Locate every blood parasite and identify its species.
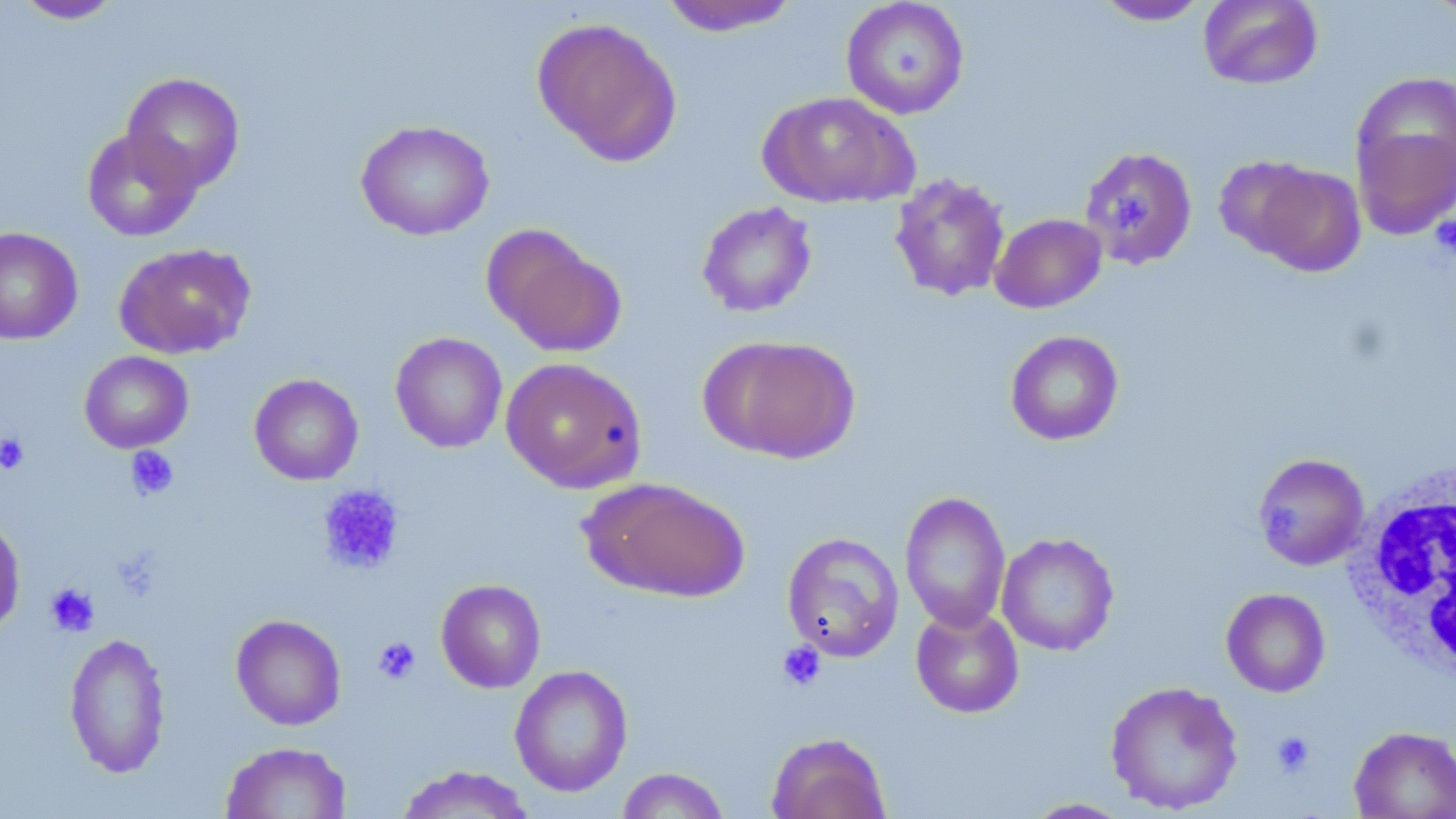
No blood parasites observed.

Approximate bounding boxes as [x1, y1, x2, y2] in pixels. Platelet locations: [1118, 192, 1161, 242], [1431, 214, 1456, 258], [0, 431, 30, 475], [126, 446, 178, 500], [317, 484, 405, 576], [44, 583, 99, 636], [373, 637, 420, 685], [777, 641, 826, 691], [1270, 730, 1316, 778]. Uninfected red blood cell locations: [12, 0, 125, 24], [1198, 0, 1324, 90], [657, 1, 804, 36], [841, 1, 970, 120], [1092, 1, 1211, 26], [532, 17, 682, 166], [122, 72, 244, 193], [1351, 89, 1456, 238], [758, 91, 916, 209], [355, 119, 494, 241], [82, 127, 202, 241], [1079, 146, 1198, 271], [1234, 159, 1366, 277], [889, 173, 1011, 302], [697, 202, 817, 317], [990, 213, 1107, 313], [481, 224, 625, 357], [0, 227, 83, 345], [113, 242, 256, 360], [1005, 330, 1124, 446], [390, 332, 508, 453], [700, 334, 860, 463], [79, 351, 193, 453], [500, 357, 647, 493], [249, 374, 363, 486], [1252, 453, 1370, 571], [582, 476, 750, 603], [899, 490, 1011, 633], [0, 515, 25, 638], [782, 532, 904, 662], [997, 532, 1119, 656], [436, 579, 546, 693], [1221, 588, 1330, 697], [910, 604, 1024, 718], [231, 614, 346, 730], [64, 631, 171, 778], [510, 665, 633, 797], [1105, 680, 1244, 815], [1349, 726, 1456, 818], [766, 732, 890, 819], [220, 741, 353, 819], [394, 765, 536, 819], [616, 767, 730, 818], [1020, 797, 1136, 818]. White blood cell locations: [1343, 463, 1456, 683]. Slide-level diagnosis: negative for blood parasites. Light microscopy. Thin blood film. May-Grünwald-Giemsa-stained preparation. Image is 1456×819 pixels. One field of a larger specimen. 1000x magnification.